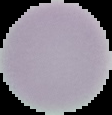

Result: negative for malaria parasites. The area outside the segmented cell region is set to black. From a thin blood film. Image is 112×115 pixels.